State which parasite is depicted.
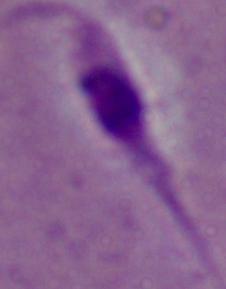

Leishmania.

Summary:
  - Modality: micrograph
  - Magnification: 1000x